Assess this cell for malaria.
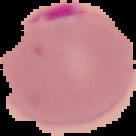

It is parasitized.

From a thin blood smear. Image is 136×136 pixels. Cell region segmented out of the field of view; the surrounding area is masked to black.